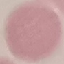

Result: no malaria parasites seen. Giemsa stain. Photographed with a smartphone camera at the microscope eyepiece. Automatically extracted cell patch, resized to 64 × 64 pixels. Thin smear of blood.